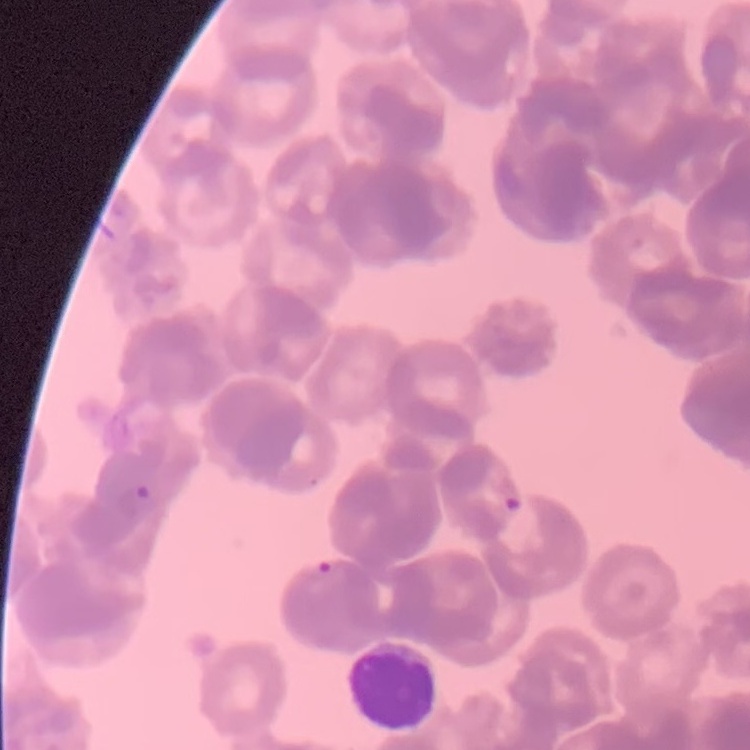
{
  "red_blood_cell_morphology": "rouleaux formation",
  "image_type": "square crop of a larger photomicrograph",
  "stain": "Field's or Giemsa",
  "preparation": "thin blood smear"
}